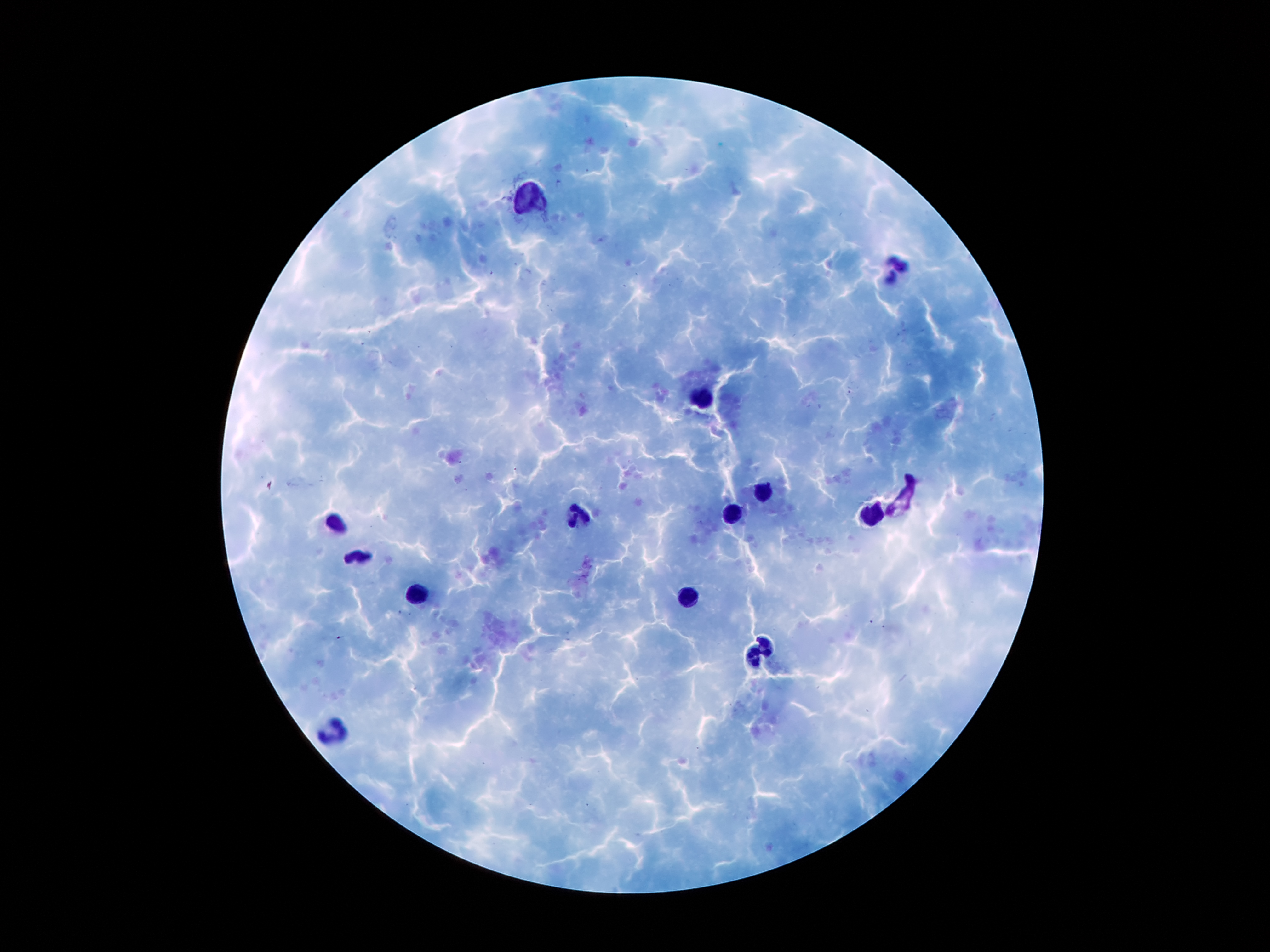

Approximate centers as (x, y) in pixels. Leukocyte locations: (530, 195), (895, 273), (704, 395), (765, 489), (734, 513), (872, 513), (583, 516), (336, 524), (358, 554), (421, 589), (690, 595), (756, 652), (336, 727). One field from this slide. Plasmodium parasites: not detected. Image is 1270×952 pixels. Thick blood smear. Giemsa stain. Patient malaria status: infected with Plasmodium falciparum. 100x magnification. Photographed through the microscope eyepiece with a smartphone camera.